Locate every blood parasite and identify its species.
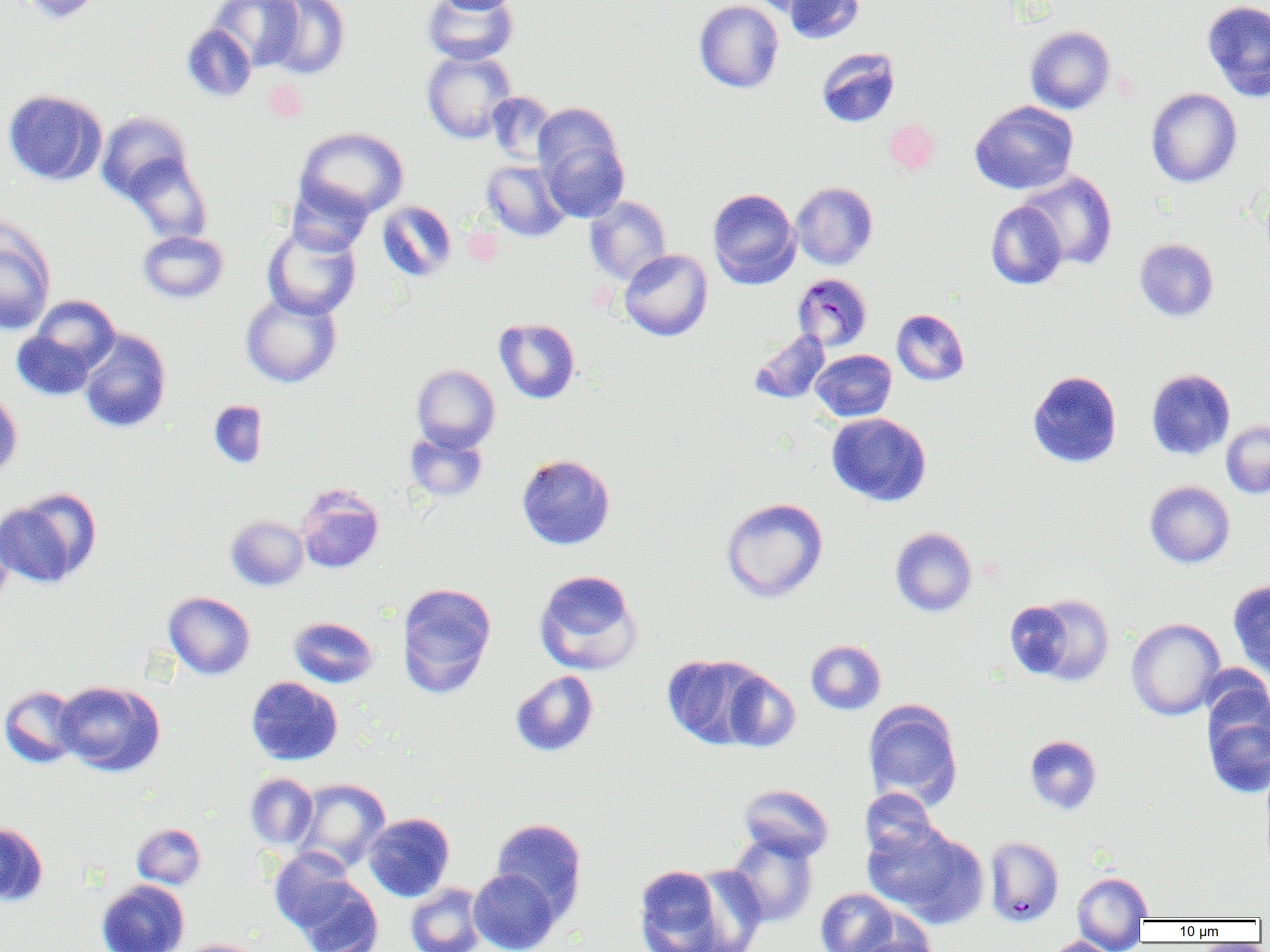

Approximate bounding boxes as (x1, y1, x2, y2) in pixels.
Plasmodium malariae-infected red blood cells: (792, 273, 872, 351).
No Plasmodium falciparum, Plasmodium ovale, Plasmodium vivax, Babesia divergens, or Trypanosoma brucei observed.

slide_level_diagnosis: Plasmodium malariae
modality: light microscopy
field_of_view: single
uninfected_red_blood_cell_locations: 'approximate bounding boxes as (x1, y1, x2, y2) in pixels: (16, 0, 105, 23), (211, 0, 304, 70), (263, 0, 350, 79), (422, 0, 519, 65), (434, 0, 519, 14), (694, 0, 784, 93), (747, 0, 826, 16), (782, 0, 864, 45), (1202, 0, 1270, 102), (181, 23, 257, 102), (1025, 25, 1115, 114), (816, 47, 900, 127), (422, 49, 516, 143), (1146, 88, 1242, 188), (3, 89, 107, 185), (486, 91, 558, 166), (970, 100, 1078, 194), (96, 111, 194, 203), (536, 117, 629, 222), (884, 119, 940, 174), (294, 127, 409, 220), (123, 154, 211, 244), (481, 160, 570, 241), (1019, 172, 1117, 270), (287, 180, 374, 255), (1260, 180, 1270, 271), (791, 182, 877, 270), (707, 188, 801, 288), (585, 195, 672, 285), (376, 200, 456, 282), (986, 202, 1068, 289), (0, 223, 55, 334), (262, 225, 361, 319), (138, 230, 228, 303), (1135, 238, 1218, 321), (619, 249, 713, 341), (240, 292, 342, 388), (27, 295, 121, 377), (891, 309, 969, 385), (494, 318, 580, 403), (11, 328, 98, 401), (79, 329, 171, 433), (749, 329, 830, 404), (811, 350, 896, 421), (412, 365, 500, 452), (1146, 369, 1235, 459), (1027, 370, 1122, 467), (0, 389, 22, 481), (208, 400, 268, 469), (826, 413, 931, 506), (1221, 421, 1270, 498), (405, 429, 488, 503), (517, 454, 615, 549), (1145, 481, 1235, 567), (296, 484, 384, 573), (0, 489, 100, 588), (720, 498, 828, 602), (225, 515, 308, 591), (0, 517, 15, 610), (890, 527, 977, 616), (534, 569, 643, 675), (1228, 579, 1270, 679), (396, 582, 496, 697), (163, 591, 255, 680), (1013, 593, 1116, 687), (289, 616, 378, 688), (1126, 618, 1225, 720), (806, 640, 886, 714), (662, 654, 769, 749), (510, 670, 598, 757), (720, 670, 801, 752), (246, 676, 343, 765), (55, 681, 165, 776), (1202, 683, 1270, 799), (0, 685, 83, 768), (863, 699, 963, 810), (1024, 735, 1101, 814), (245, 773, 318, 850), (292, 778, 390, 872), (739, 784, 833, 861), (859, 788, 939, 862), (363, 813, 454, 901), (491, 818, 587, 920), (0, 821, 48, 907), (863, 822, 987, 928), (132, 823, 205, 889), (726, 832, 818, 927), (984, 836, 1064, 927), (269, 849, 362, 935), (633, 863, 733, 951), (683, 865, 769, 950), (469, 868, 561, 952), (1072, 871, 1153, 948), (288, 872, 385, 952), (96, 880, 189, 952), (405, 882, 486, 952), (815, 888, 899, 952), (850, 930, 939, 952), (1042, 936, 1120, 952), (175, 939, 267, 952)'
magnification: 1000x
preparation: thin blood film
image_size: 1270×952 pixels